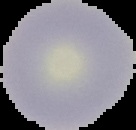
image size = 136×130 pixels
preparation = thin blood film
malaria status = uninfected
image type = segmented cell region on a black background